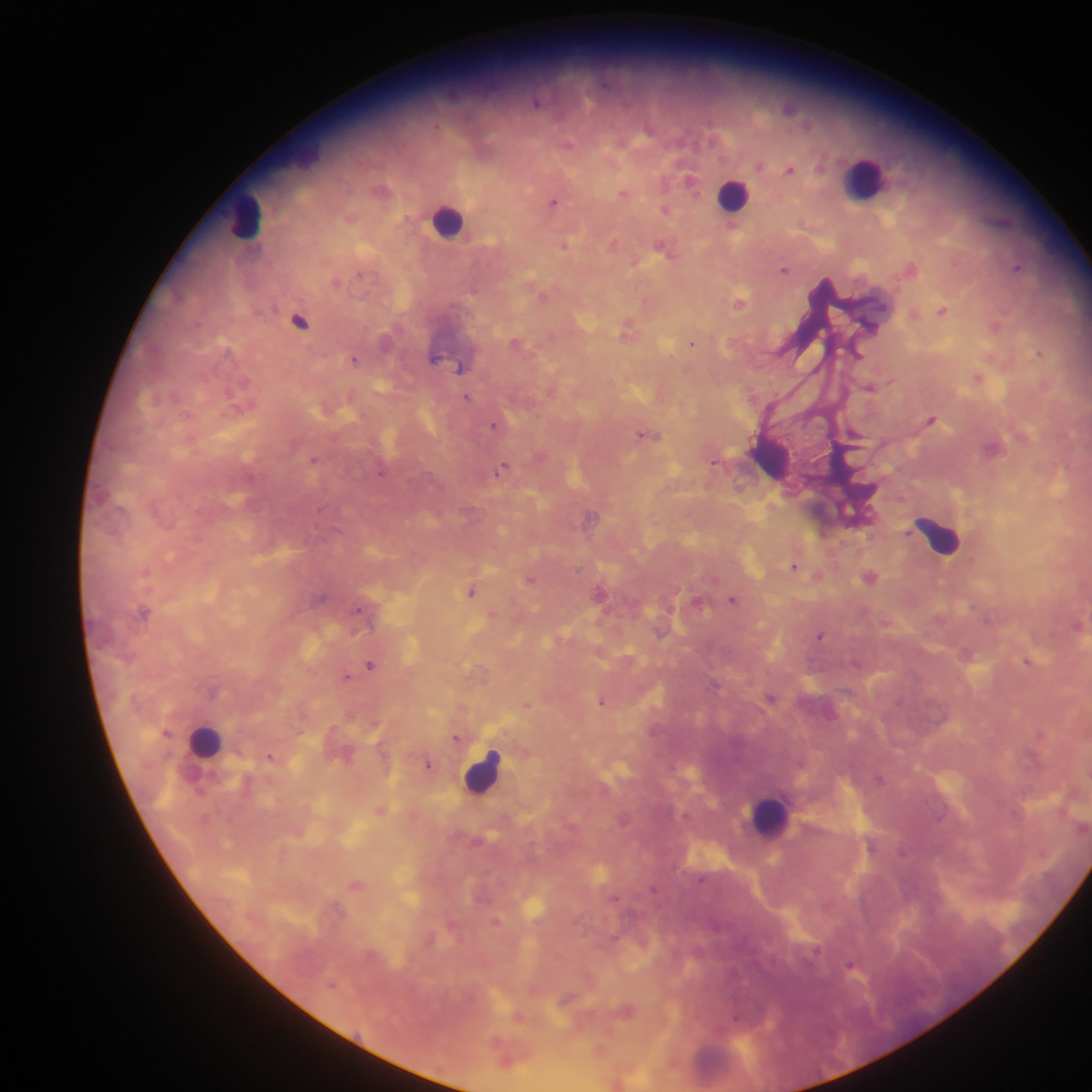
Approximate centers as x y in pixels. Malaria parasite locations: 538 101; 567 144; 790 169; 690 182; 623 193; 554 201; 666 210; 732 226; 613 242; 565 245; 662 246; 1017 267; 911 268; 784 269; 740 301; 942 310; 300 320; 868 325; 995 326; 627 327; 515 342; 692 344; 857 353; 1038 353; 435 358; 354 360; 460 367; 977 378; 869 387; 467 397; 931 420; 493 425; 854 433; 644 434; 313 460; 714 462; 501 469; 794 566; 870 577; 529 580; 471 591; 599 593; 732 599; 697 602; 358 610; 144 612; 1077 625; 820 636; 1028 661; 370 665; 346 677; 716 685; 770 697; 601 701; 526 705; 456 738; 269 757; 428 765; 880 779; 654 888; 615 898; 817 951; 851 966; 736 1015. Leukocyte locations: 865 178; 734 195; 246 216; 449 221; 939 536; 206 740; 482 772; 772 816. Single field of view. Photographed through a microscope with a mobile-phone camera. Sample from Ghana. Image is 1092×1092 pixels. Thick blood smear.